Classify this cell by malaria status.
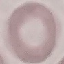

Uninfected.

Automatically extracted cell patch, resized to 64 × 64 pixels. Thin blood film. Giemsa stain. Acquired by smartphone through the microscope eyepiece.